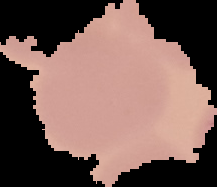

Summary:
  - Result: no Plasmodium parasites detected
  - Image type: cell region segmented out of the field of view; surrounding area masked to black
  - Image size: 217×187 pixels
  - Preparation: thin blood film